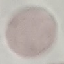
Summary:
  - Malaria status: uninfected
  - Capture: smartphone through the microscope eyepiece
  - Stain: Giemsa
  - Image type: cell patch, automatically extracted from a larger field of view and resized to 64 × 64 pixels
  - Preparation: thin blood film